Outline each Plasmodium falciparum-infected red blood cell.
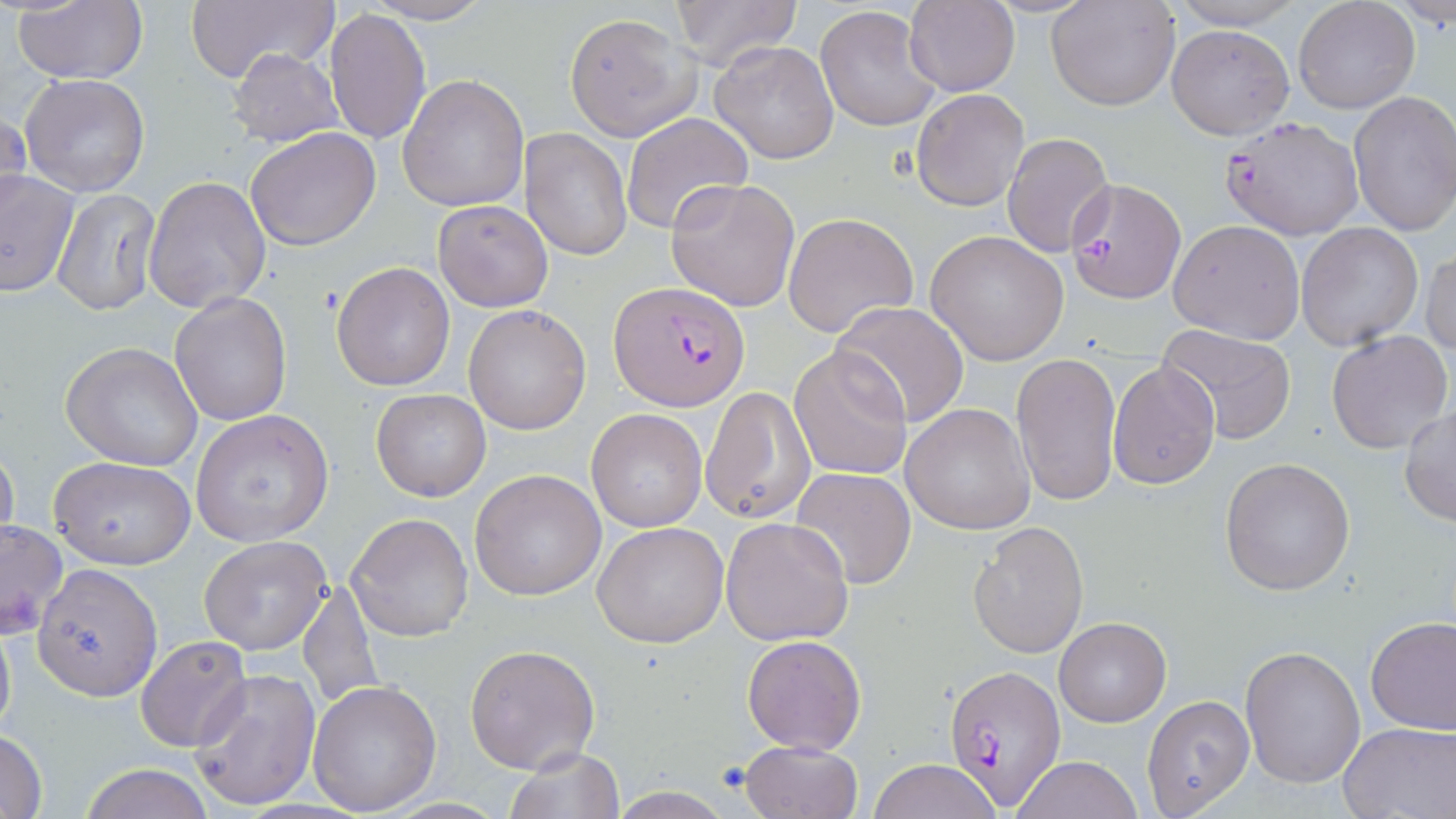

Approximate bounding boxes as (x1, y1, x2, y2) in pixels.
Plasmodium falciparum-infected red blood cells: (1219, 115, 1365, 241), (1065, 177, 1184, 303), (610, 282, 749, 412), (943, 661, 1068, 811).

slide-level diagnosis = Plasmodium falciparum
field of view = single
magnification = 1000x
uninfected red blood cell locations = approximate bounding boxes as (x1, y1, x2, y2) in pixels: (12, 0, 150, 85), (184, 0, 337, 87), (668, 0, 801, 71), (1161, 0, 1309, 29), (362, 1, 494, 25), (905, 1, 1019, 96), (1045, 1, 1180, 112), (1292, 1, 1420, 115), (1391, 3, 1456, 31), (815, 4, 941, 132), (325, 8, 430, 145), (563, 13, 700, 141), (1167, 23, 1294, 139), (708, 39, 839, 165), (227, 47, 344, 148), (19, 73, 150, 195), (398, 75, 530, 210), (912, 89, 1029, 211), (1348, 91, 1456, 236), (0, 106, 30, 224), (621, 113, 752, 236), (245, 127, 381, 251), (521, 129, 632, 260), (1002, 132, 1114, 259), (0, 170, 77, 299), (144, 176, 272, 313), (666, 177, 800, 311), (51, 187, 163, 317), (433, 199, 554, 313), (783, 212, 917, 338), (1168, 220, 1306, 345), (1295, 223, 1423, 354), (925, 230, 1068, 366), (1420, 249, 1455, 359), (331, 261, 457, 392), (167, 292, 292, 428), (831, 301, 970, 429), (463, 306, 590, 435), (1155, 325, 1298, 444), (1326, 330, 1454, 457), (60, 342, 204, 471), (789, 347, 914, 481), (1010, 353, 1122, 507), (1108, 361, 1220, 490), (701, 387, 814, 526), (370, 389, 491, 501), (901, 403, 1037, 535), (1399, 405, 1455, 528), (587, 407, 709, 532), (191, 409, 334, 547), (0, 445, 21, 558), (50, 456, 195, 570), (1220, 456, 1355, 595), (790, 466, 914, 590), (470, 469, 606, 599), (346, 513, 473, 642), (721, 516, 854, 646), (0, 520, 68, 638), (966, 520, 1090, 657), (593, 521, 730, 648), (199, 536, 333, 655), (34, 565, 161, 700), (297, 576, 383, 715), (0, 613, 17, 749), (1365, 615, 1456, 736), (1054, 616, 1171, 727), (741, 634, 867, 756), (136, 636, 251, 752), (466, 644, 602, 775), (1241, 644, 1367, 787), (190, 671, 320, 809), (307, 680, 441, 816), (1141, 694, 1255, 818), (1337, 721, 1456, 818), (0, 730, 49, 818), (739, 739, 864, 819), (505, 745, 624, 818), (1009, 756, 1142, 819), (868, 759, 1001, 819), (77, 765, 218, 819), (605, 788, 736, 818)
stain = May-Grünwald-Giemsa
preparation = thin blood film
image size = 1456×819 pixels
modality = optical microscopy